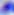
Summary:
  - Identification: Toxoplasma gondii
  - Magnification: 400x
  - Modality: photomicrograph